Identify the parasite.
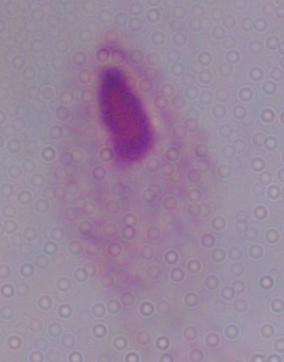

This is a trichomonad.

Summary:
  - Magnification: 1000x
  - Modality: micrograph